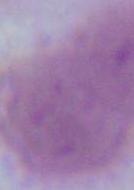
magnification = 1000x
modality = photomicrograph
identification = red blood cell